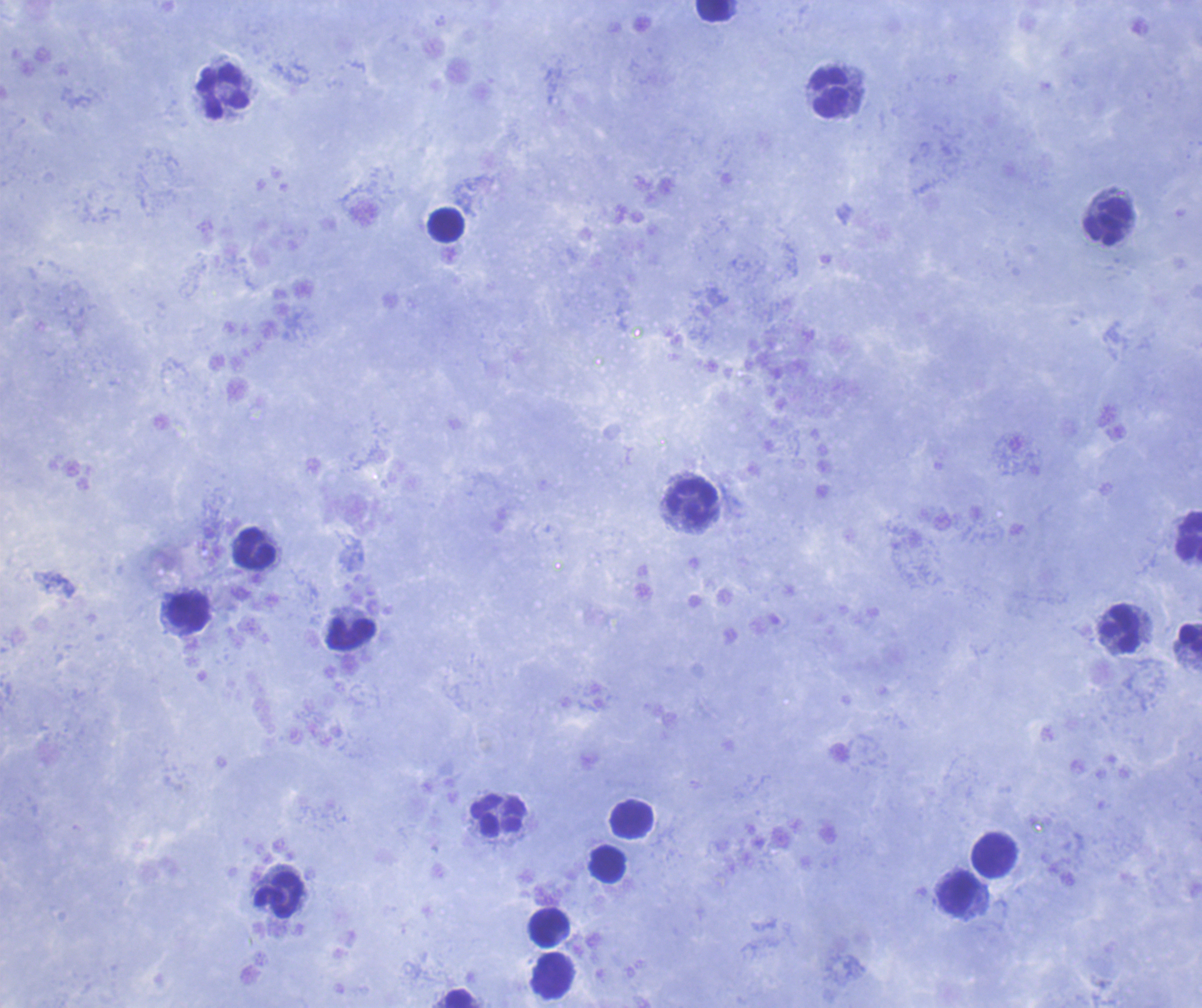

Approximate centers as {x, y} in pixels. Leukocyte locations: {713, 11}, {223, 92}, {830, 92}, {1108, 223}, {446, 226}, {690, 502}, {1188, 535}, {254, 549}, {190, 612}, {1119, 629}, {350, 634}, {1189, 640}, {499, 816}, {632, 819}, {994, 854}, {607, 865}, {958, 894}, {279, 896}, {549, 927}, {553, 975}, {461, 999}. Result: no malaria parasites seen. Image is 1202×1008 pixels. Romanowsky stain. 100x magnification. Background quality: good. Previously used in a real diagnosis. Thick blood smear. Coloration quality: good. Single field of view.